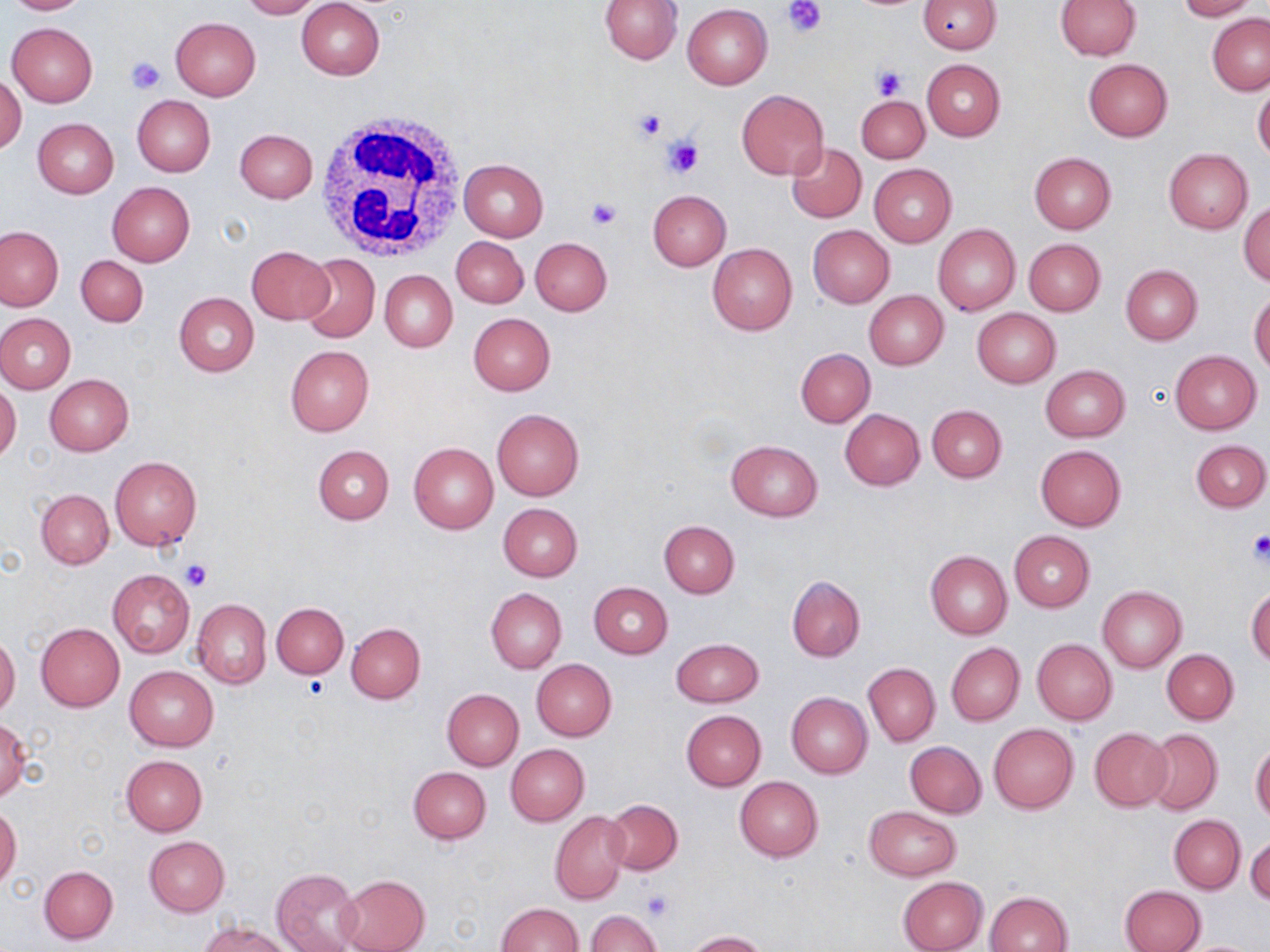 Approximate bounding boxes as (x1,y1)-(x2,y2) corner pairs in pixels. Uninfected red blood cell locations: (1,0)-(93,15), (237,0)-(321,19), (296,0)-(386,79), (599,0)-(683,64), (1055,0)-(1141,60), (1175,0)-(1256,21), (919,1)-(1000,53), (682,4)-(772,89), (1208,13)-(1270,95), (170,17)-(261,100), (6,22)-(97,106), (1083,58)-(1172,141), (922,59)-(1005,140), (1,73)-(26,155), (1253,82)-(1270,163), (736,88)-(829,180), (133,95)-(215,177), (856,96)-(930,164), (33,118)-(119,197), (234,128)-(318,203), (785,143)-(867,223), (1164,149)-(1252,234), (1029,152)-(1116,234), (458,159)-(548,241), (869,164)-(957,248), (106,182)-(195,267), (647,189)-(731,271), (1239,201)-(1270,287), (933,223)-(1020,315), (808,225)-(895,307), (0,226)-(64,311), (451,237)-(528,308), (531,237)-(612,315), (1023,238)-(1106,316), (707,243)-(797,335), (246,246)-(333,324), (297,252)-(381,344), (76,254)-(148,327), (1120,265)-(1202,345), (380,271)-(457,352), (864,290)-(949,369), (1249,292)-(1270,373), (175,293)-(259,377), (972,307)-(1060,387), (0,313)-(75,393), (468,313)-(555,395), (286,346)-(374,437), (795,347)-(875,427), (1170,349)-(1261,434), (1039,365)-(1130,442), (44,374)-(134,455), (0,383)-(21,465), (927,404)-(1007,482), (840,409)-(925,490), (492,410)-(584,501), (1191,439)-(1270,512), (726,440)-(822,520), (409,442)-(498,533), (312,444)-(394,524), (1035,445)-(1126,530), (109,457)-(202,550), (37,489)-(113,568), (498,503)-(583,582), (659,521)-(739,597), (1009,531)-(1094,611), (925,551)-(1012,639), (107,569)-(195,659), (788,575)-(864,661), (589,583)-(673,659), (1097,586)-(1187,672), (1245,586)-(1270,668), (486,588)-(567,673), (191,598)-(271,688), (272,602)-(349,678), (346,622)-(425,703), (36,623)-(125,710), (0,634)-(20,719), (672,639)-(763,707), (1032,639)-(1117,724), (947,642)-(1024,726), (1162,649)-(1238,723), (532,659)-(616,741), (863,662)-(940,746), (125,666)-(218,751), (442,689)-(523,770), (786,692)-(871,779), (681,710)-(766,790), (0,716)-(31,802), (989,722)-(1079,813), (1088,727)-(1172,811), (1144,729)-(1223,815), (905,741)-(987,818), (1250,741)-(1270,821), (506,744)-(589,825), (131,751)-(214,912), (121,755)-(206,837), (407,765)-(491,844), (735,777)-(824,861), (604,799)-(683,875), (0,804)-(21,889), (864,806)-(962,881), (550,811)-(629,904), (1170,815)-(1246,892), (1247,832)-(1270,906), (144,837)-(229,916), (39,865)-(118,944), (271,869)-(363,952), (338,874)-(430,952), (897,876)-(988,952), (1121,885)-(1205,952), (986,890)-(1073,952), (495,902)-(583,952), (587,910)-(662,952), (199,920)-(292,952), (686,930)-(767,951). Platelet locations: (784,0)-(828,38), (127,57)-(165,94), (871,64)-(909,100), (632,106)-(668,143), (662,135)-(704,179), (586,199)-(621,230), (1245,532)-(1270,566), (181,559)-(213,590), (302,676)-(327,698), (641,889)-(672,921). White blood cell locations: (314,110)-(470,262). Slide-level diagnosis: no evidence of blood parasites. Captured at 1000x magnification. Image is 1270×952 pixels. Light microscopy. Thin blood film. Single field of view. May-Grünwald-Giemsa stain.